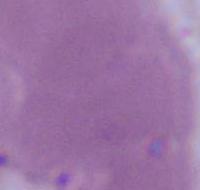

identification = red blood cell
magnification = 1000x
modality = photomicrograph